Name the parasite shown.
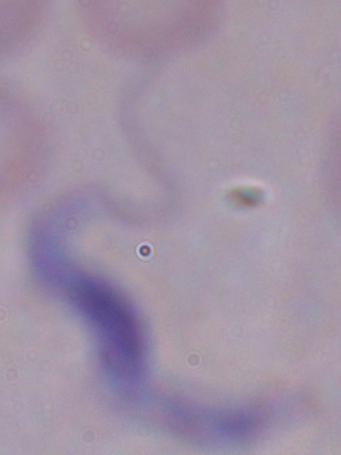

This is a trypanosome.

{
  "modality": "photomicrograph",
  "magnification": "1000x"
}